State which parasite is depicted.
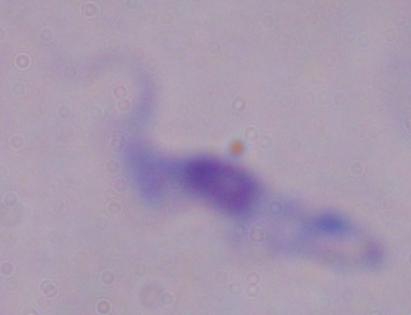
A trypanosome.

Summary:
  - Modality: photomicrograph
  - Magnification: 1000x